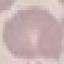

result = no malaria parasites seen
stain = Giemsa
image type = automatically extracted cell patch, resized to 64 × 64 pixels
capture = smartphone through the microscope eyepiece
preparation = thin blood film